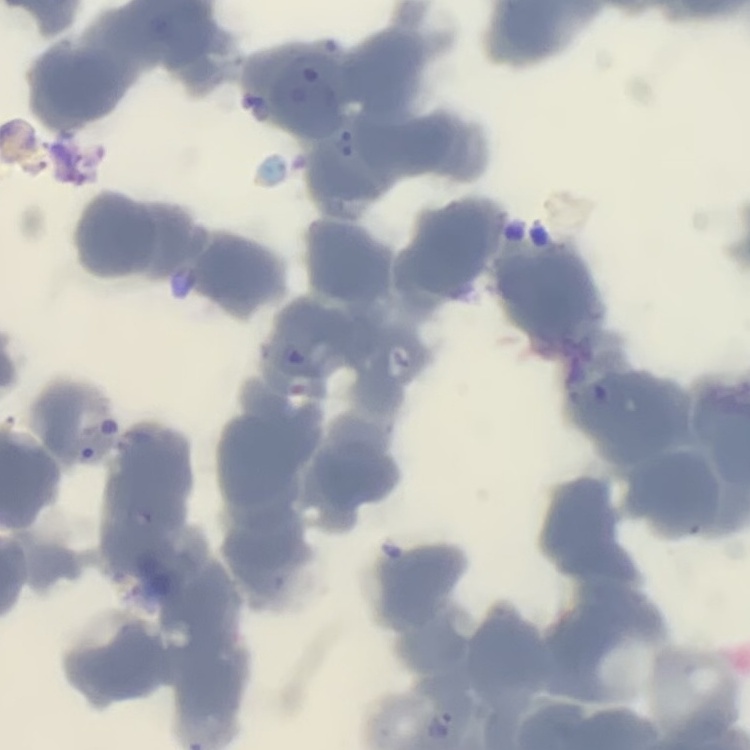

red_blood_cell_morphology: rouleaux formation
stain: Field's or Giemsa
preparation: thin blood smear
image_type: one tile cut from a larger photomicrograph